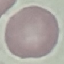
malaria status = uninfected
stain = Giemsa
preparation = thin blood film
capture = smartphone through the microscope eyepiece
image type = automatically extracted cell patch, resized to 64 × 64 pixels